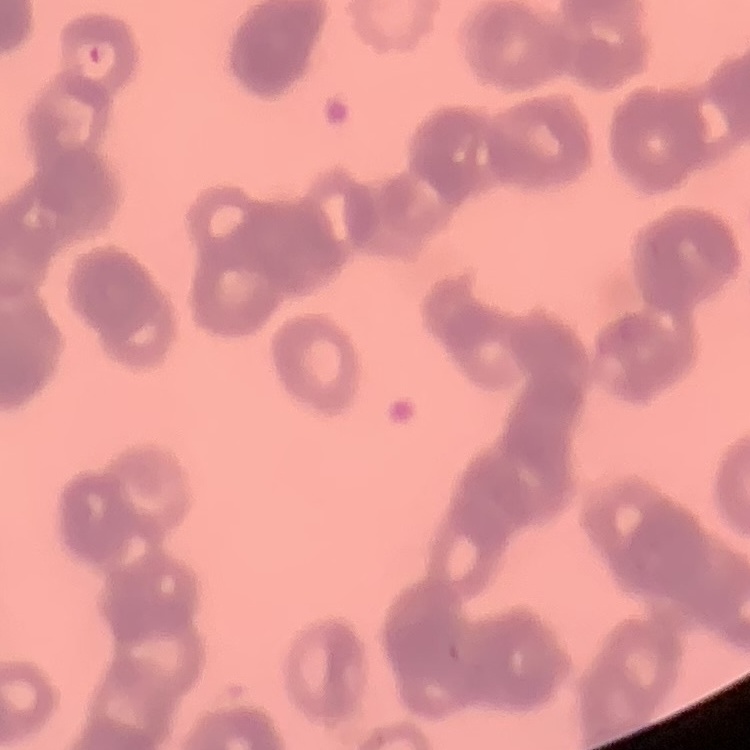 The erythrocytes show rouleaux formation. Thin peripheral smear. One tile cut from a larger photomicrograph. Field's or Giemsa stain.